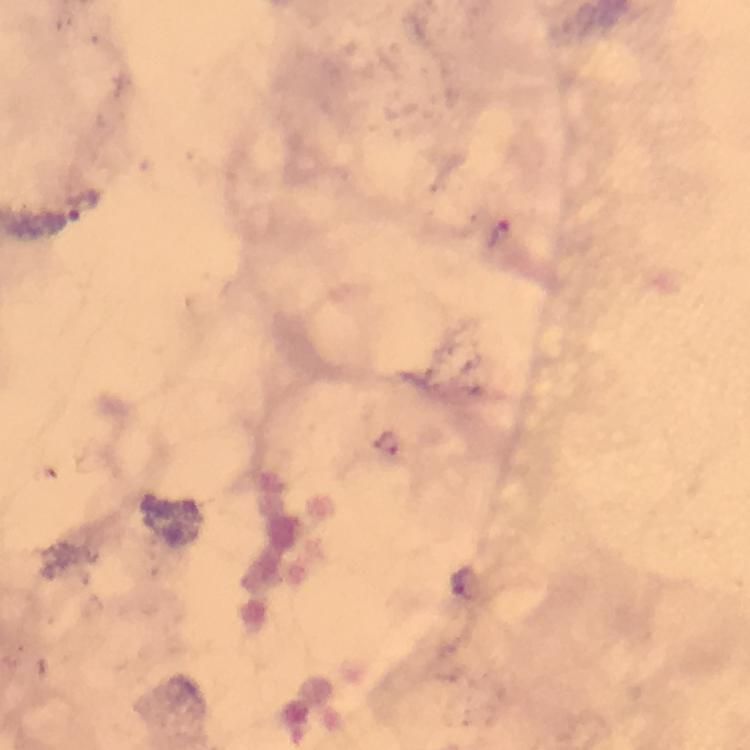
Approximate centers as [x, y] in pixels.
Summary:
  - Malaria parasite locations: [83, 205], [500, 237], [466, 583]
  - Context: from a malaria diagnostic workup
  - Stain: Giemsa
  - Immersion oil: applied
  - Preparation: thick blood smear
  - Cropped from: one field of view
  - Capture: smartphone mounted on the microscope
  - Image size: 750×750 pixels
  - Magnification: 100x